Locate every blood parasite and identify its species.
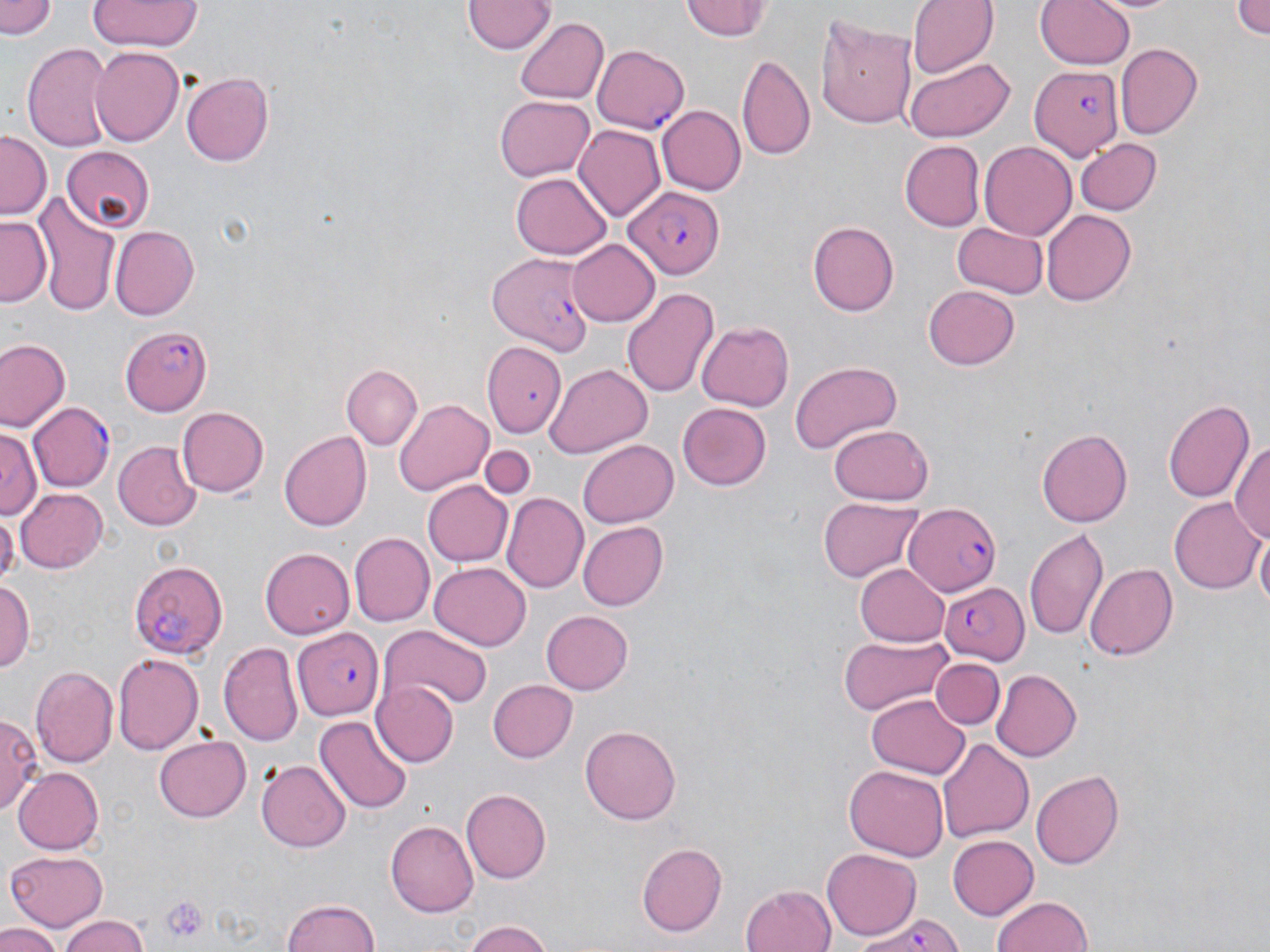

Approximate bounding boxes as (x1,y1)-(x2,y2) corner pairs in pixels.
Plasmodium falciparum-infected red blood cells: (593,45)-(689,134), (1030,66)-(1124,160), (622,185)-(724,277), (487,252)-(591,355), (119,326)-(213,417), (28,403)-(114,492), (902,503)-(1003,594), (127,559)-(230,658), (939,579)-(1032,664), (294,628)-(383,720), (850,910)-(968,951).
No Plasmodium ovale, Plasmodium malariae, Plasmodium vivax, Babesia divergens, or Trypanosoma brucei observed.

slide_level_diagnosis: Plasmodium falciparum
uninfected_red_blood_cell_locations: 'approximate bounding boxes as (x1,y1)-(x2,y2) corner pairs in pixels: (2,0)-(59,41), (88,0)-(201,53), (677,0)-(778,42), (907,0)-(998,78), (1035,0)-(1137,71), (1087,0)-(1186,14), (1231,0)-(1270,39), (462,1)-(553,54), (814,11)-(918,132), (516,17)-(609,106), (22,42)-(114,152), (1115,43)-(1201,138), (90,47)-(183,148), (737,52)-(815,160), (902,56)-(1016,142), (180,71)-(276,167), (494,95)-(594,182), (657,105)-(744,195), (575,127)-(665,221), (0,129)-(52,217), (1075,138)-(1161,216), (899,140)-(985,232), (980,143)-(1076,238), (61,147)-(155,232), (513,171)-(612,259), (34,188)-(119,311), (1042,210)-(1137,306), (0,215)-(51,305), (806,220)-(900,315), (952,223)-(1047,298), (110,226)-(200,320), (565,238)-(659,327), (923,284)-(1019,371), (622,286)-(719,402), (698,322)-(794,410), (1,338)-(69,432), (485,341)-(564,436), (790,361)-(903,455), (341,364)-(422,451), (544,364)-(651,460), (393,397)-(493,497), (1165,397)-(1256,502), (678,403)-(772,491), (176,405)-(268,498), (827,425)-(934,505), (1035,427)-(1133,526), (1,428)-(41,521), (279,431)-(371,531), (1231,433)-(1270,547), (113,440)-(199,530), (578,440)-(678,527), (479,445)-(535,499), (423,478)-(512,564), (14,485)-(107,573), (503,493)-(588,591), (1170,496)-(1263,596), (819,497)-(925,583), (0,512)-(17,586), (578,521)-(668,611), (1255,526)-(1269,617), (1025,527)-(1109,640), (348,532)-(434,627), (261,547)-(355,639), (430,561)-(532,649), (855,561)-(950,647), (1087,563)-(1178,661), (0,578)-(35,673), (541,611)-(634,694), (379,625)-(493,711), (836,636)-(953,715), (219,641)-(304,748), (112,653)-(204,754), (931,656)-(1003,728), (28,664)-(117,768), (992,669)-(1082,761), (487,678)-(577,762), (375,679)-(458,767), (867,693)-(970,778), (2,713)-(42,817), (314,713)-(412,812), (580,724)-(682,825), (154,736)-(250,821), (937,738)-(1033,844), (256,760)-(350,851), (843,763)-(948,860), (12,766)-(102,855), (1031,768)-(1125,870), (462,788)-(551,882), (386,820)-(479,914), (947,834)-(1039,919), (635,842)-(729,937), (823,847)-(922,939), (6,848)-(109,931), (740,882)-(837,952), (990,894)-(1094,952), (280,897)-(383,952), (55,913)-(153,952), (458,920)-(559,952), (0,924)-(62,952)'
modality: light microscopy
platelet_locations: 'approximate bounding boxes as (x1,y1)-(x2,y2) corner pairs in pixels: (159,894)-(209,944)'
stain: May-Grünwald-Giemsa
preparation: thin blood smear
field_of_view: single
image_size: 1270×952 pixels
magnification: 1000x